State which parasite is depicted.
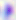

Toxoplasma gondii.

magnification = 400x
modality = micrograph